Point out each Plasmodium parasite.
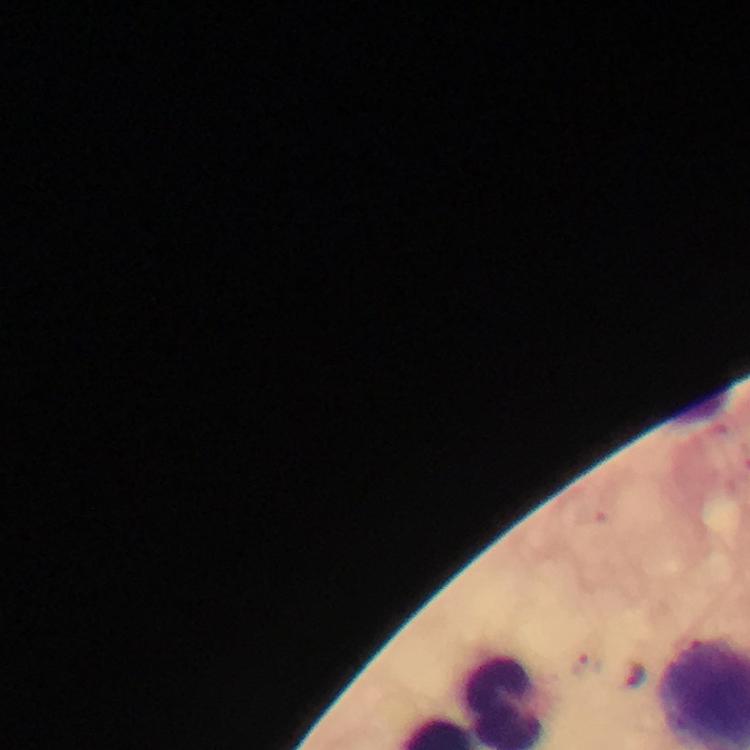

Approximate centers as {x, y} in pixels.
Plasmodium parasites: {588, 665}, {631, 673}.

Summary:
  - Capture: smartphone mounted on the microscope
  - Context: from a diagnostic examination for malaria
  - Stain: Giemsa
  - Cropped from: one field of view
  - Preparation: thick blood film
  - Immersion oil: used
  - Magnification: 100x
  - Image size: 750×750 pixels